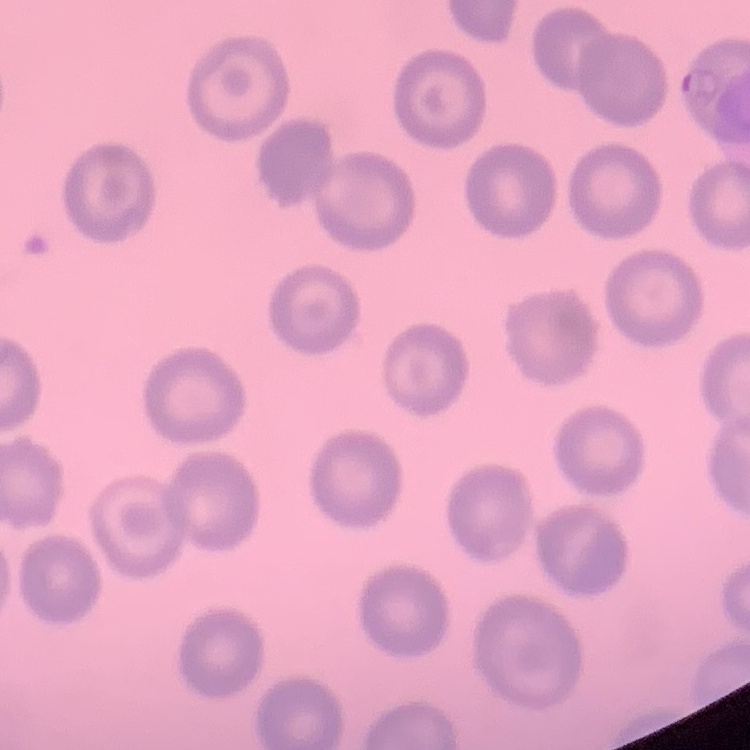
The erythrocytes exhibit no rouleaux formation. Thin blood smear. One tile cut from a larger photomicrograph. Stained with either Field's or Giemsa.